Look for Plasmodium parasites.
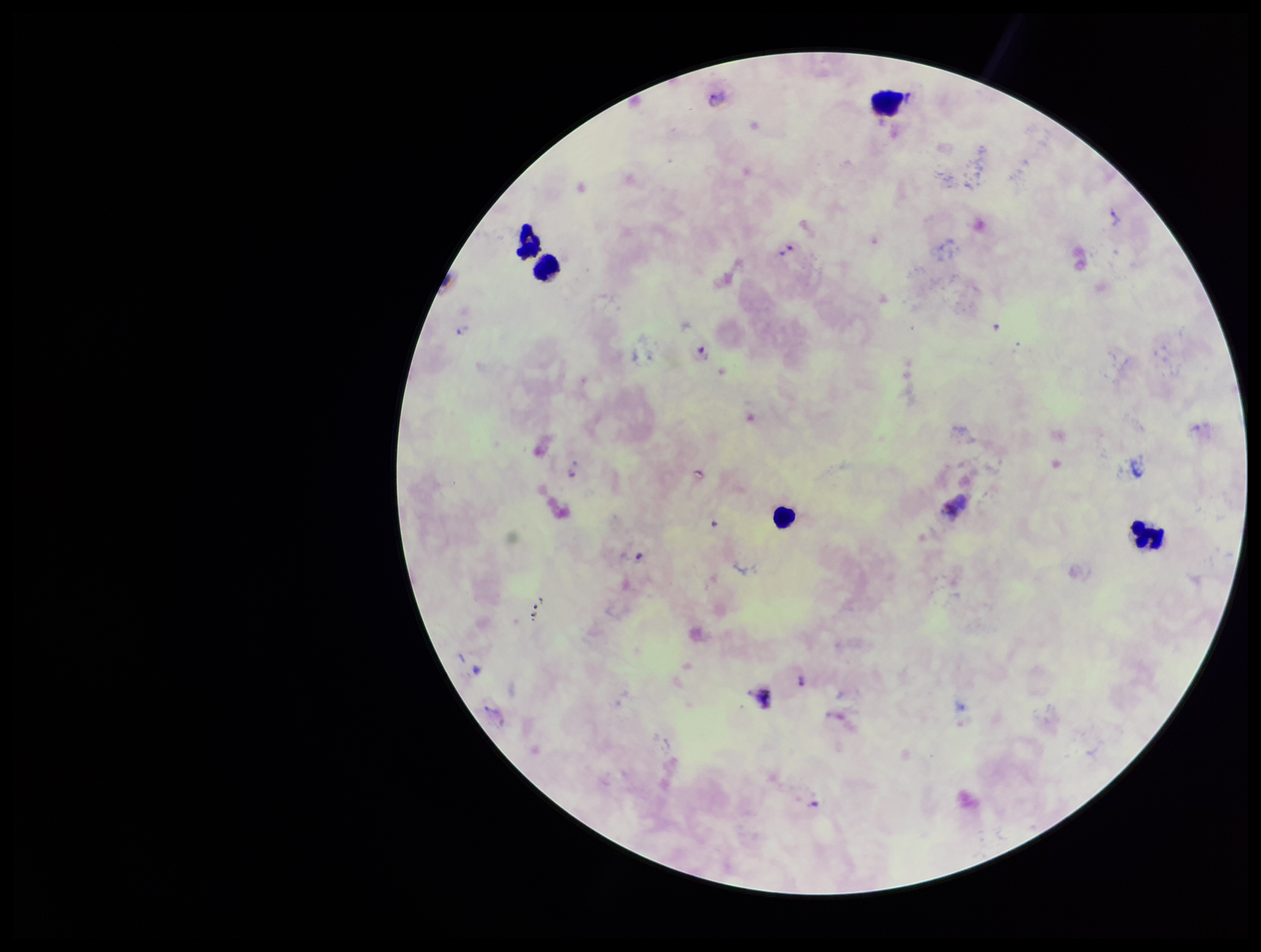
Seen.

image size = 1261×952 pixels
field of view = single
capture = smartphone photograph through the microscope eyepiece
parasite count = 8
species reported for this patient = Plasmodium vivax
preparation = thick
patient malaria status = infected
stain = Giemsa
leukocyte count = 5